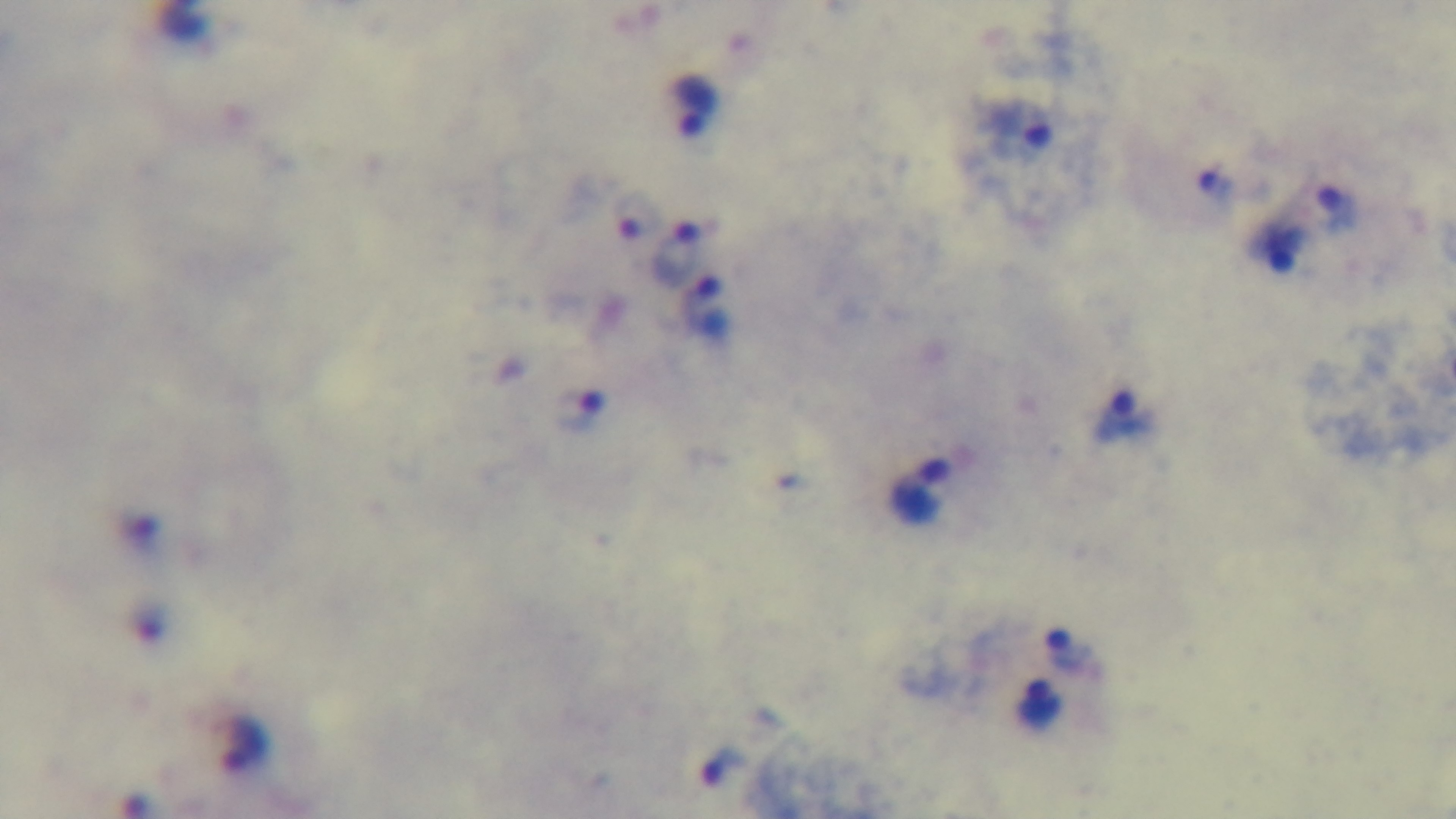

Summary:
  - Preparation: thick blood film
  - Malaria status: positive
  - Stain: Giemsa
  - Capture: mounted 4K digital camera
  - Objective: 100x oil immersion
  - Modality: light microscopy
  - Field of view: single